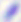

Summary:
  - Magnification: 400x
  - Identification: Toxoplasma gondii
  - Modality: photomicrograph